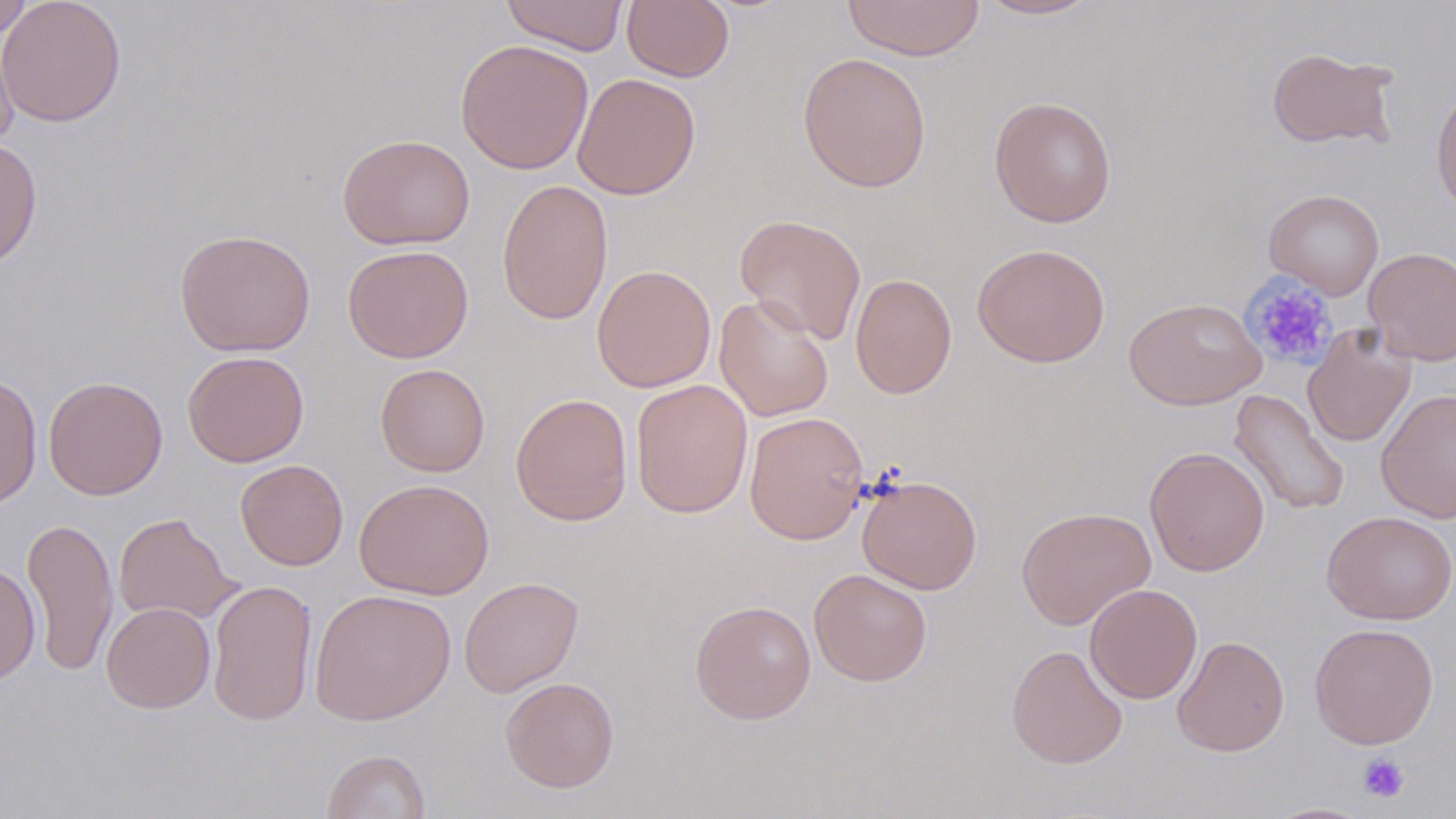

Approximate bounding boxes as [x1, y1, x2, y2] in pixels. Uninfected red blood cell locations: [0, 0, 127, 128], [501, 0, 628, 56], [842, 0, 985, 61], [973, 0, 1105, 20], [0, 1, 35, 40], [621, 1, 735, 82], [0, 22, 19, 151], [455, 39, 594, 175], [1266, 45, 1400, 151], [797, 51, 932, 193], [572, 72, 701, 200], [1430, 81, 1456, 220], [989, 96, 1117, 227], [337, 133, 475, 250], [0, 138, 42, 269], [497, 179, 613, 326], [1264, 189, 1384, 299], [734, 213, 867, 344], [174, 228, 316, 357], [972, 242, 1110, 367], [342, 244, 473, 363], [1363, 247, 1456, 366], [591, 264, 716, 392], [850, 273, 957, 399], [713, 294, 833, 422], [1125, 296, 1266, 410], [1302, 324, 1417, 448], [182, 350, 309, 467], [375, 363, 490, 477], [1, 374, 42, 509], [43, 375, 168, 500], [630, 379, 753, 519], [1376, 387, 1456, 524], [1229, 389, 1350, 516], [510, 393, 633, 526], [744, 411, 869, 544], [1144, 446, 1270, 577], [235, 459, 348, 571], [856, 474, 982, 594], [354, 478, 494, 600], [1016, 506, 1156, 630], [1321, 510, 1456, 625], [113, 512, 241, 626], [21, 517, 119, 676], [0, 562, 40, 685], [808, 568, 932, 687], [459, 577, 584, 697], [207, 578, 318, 726], [1084, 584, 1203, 704], [309, 588, 456, 726], [689, 599, 817, 724], [101, 602, 216, 713], [1309, 622, 1439, 748], [1172, 635, 1290, 757], [1006, 643, 1128, 769], [500, 676, 619, 793], [321, 749, 431, 819], [1261, 801, 1377, 818]. Platelet locations: [1240, 274, 1338, 371], [1357, 753, 1410, 803]. Slide-level diagnosis: negative for blood parasites. Optical microscopy. Thin blood film. Image is 1456×819 pixels. Captured at 1000x magnification. Single field of view. May-Grünwald-Giemsa-stained preparation.